Name the parasite shown.
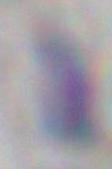
This is Toxoplasma gondii.

modality: photomicrograph
magnification: 1000x